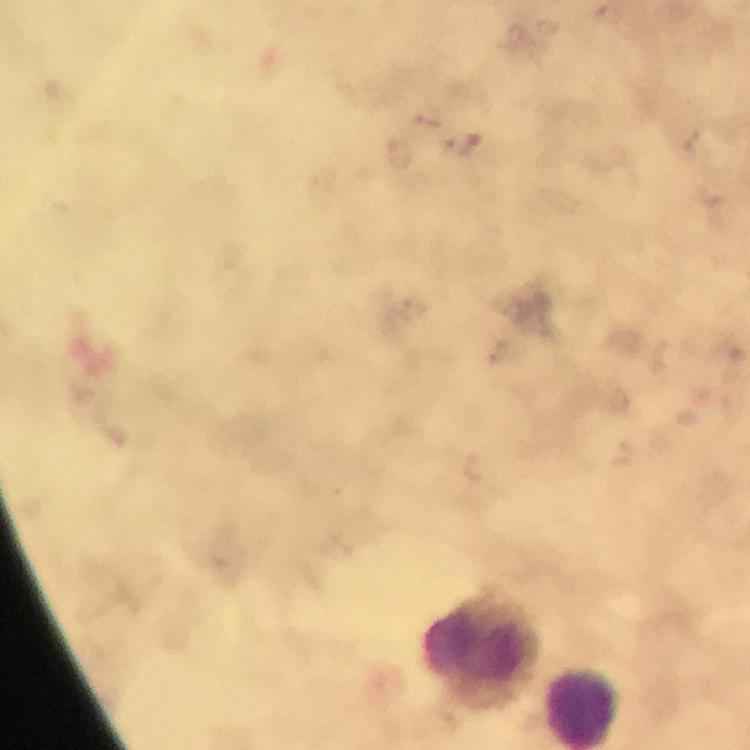
Approximate centers as [x, y] in pixels. Malaria parasite locations: [431, 118], [464, 144]. Leukocyte locations: [482, 651]. Image is 750×750 pixels. Smartphone photograph taken through a microscope. 100x magnification. Cropped region of a single field of view. From a malaria diagnostic workup. Thick smear. Immersion oil applied. Giemsa-stained preparation.